State the preparation type.
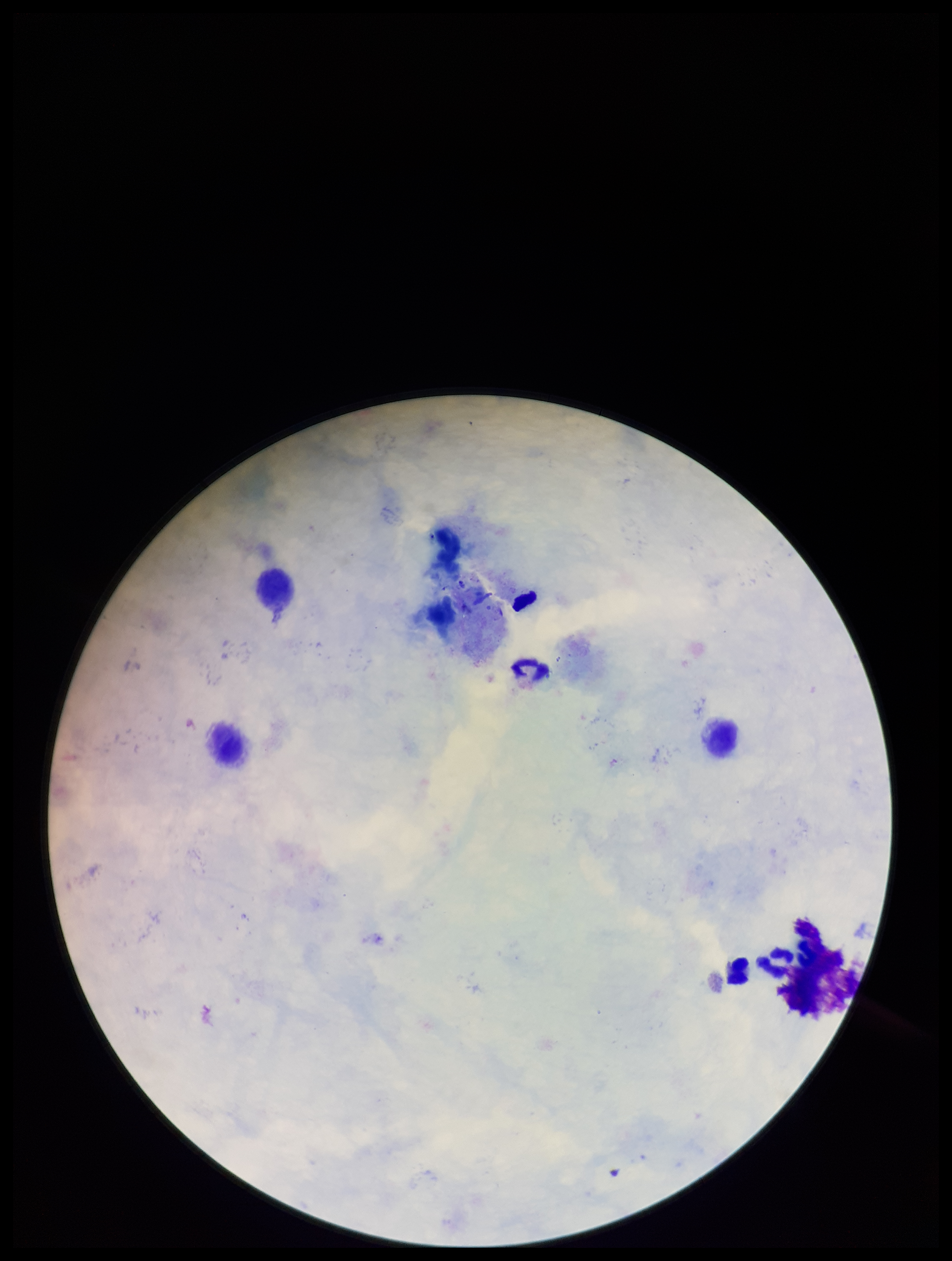

Thick.

patient malaria status = negative
parasite count = 0
capture = smartphone photograph through the microscope eyepiece
field of view = one from this slide
Plasmodium parasites = none detected
stain = Giemsa
leukocyte count = 4
image size = 952×1261 pixels